Comment on the morphology of the erythrocytes.
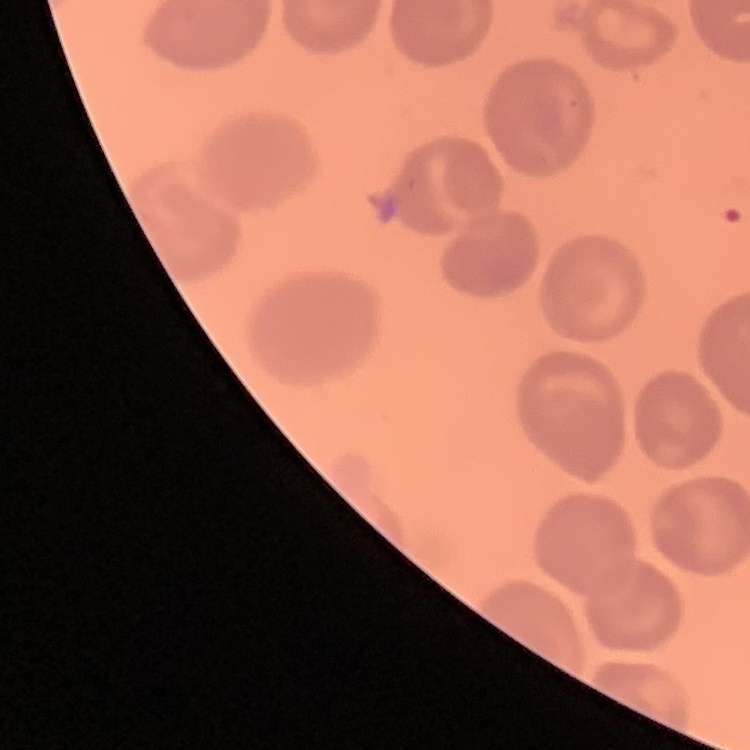

No rouleaux formation.

image type = square crop of a larger photomicrograph
preparation = thin blood smear
stain = Field's or Giemsa